Point out each Plasmodium parasite.
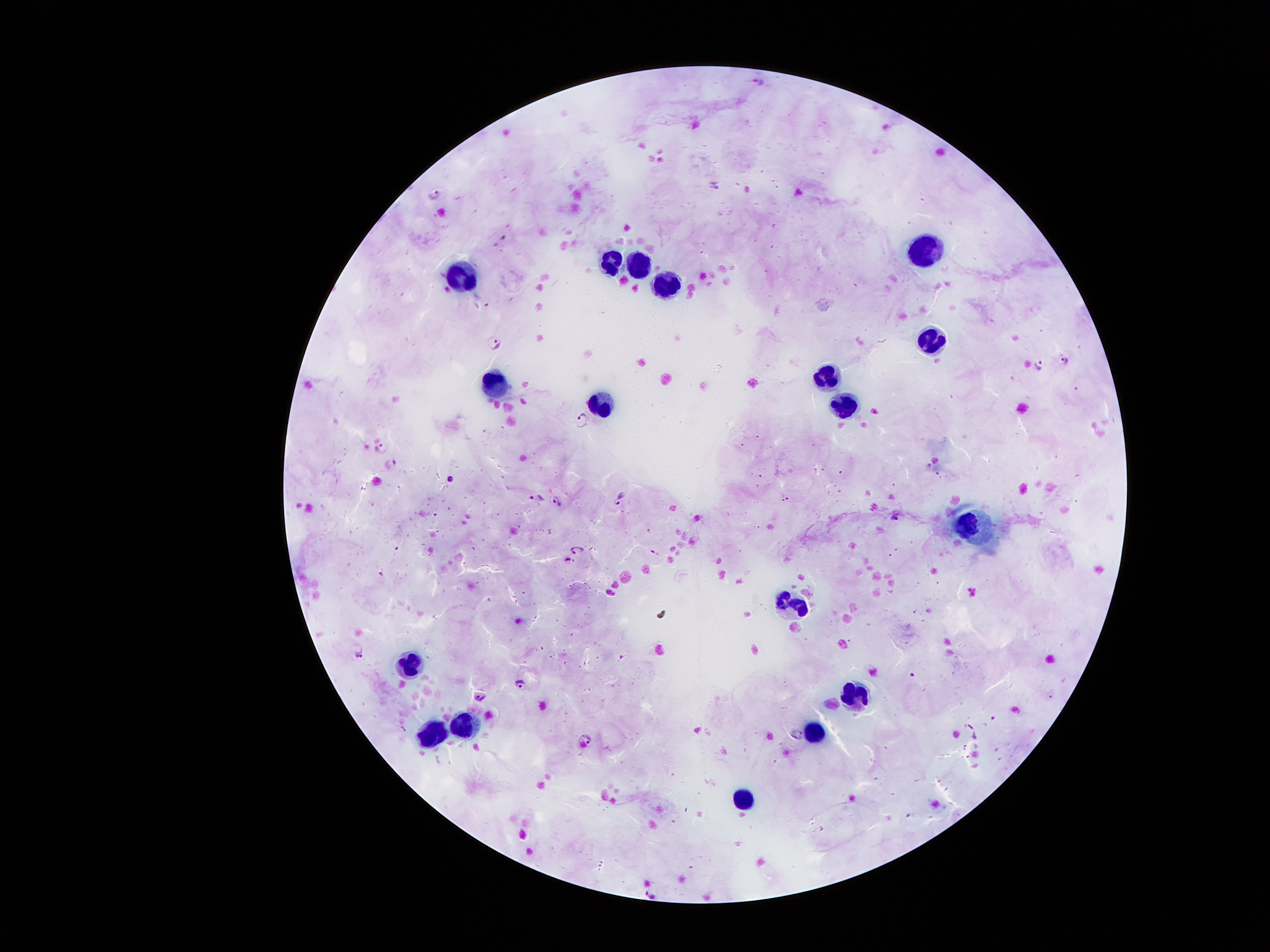

Approximate object centers, in pixels from the top-left corner.
Plasmodium parasites: (x=758, y=81), (x=713, y=183), (x=435, y=193), (x=495, y=341), (x=1064, y=360), (x=1039, y=364), (x=579, y=421), (x=384, y=450), (x=393, y=462), (x=536, y=497), (x=620, y=500), (x=558, y=503), (x=896, y=514), (x=577, y=550), (x=359, y=651), (x=519, y=683), (x=478, y=697), (x=585, y=741).

Summary:
  - Leukocyte locations: (x=931, y=250), (x=610, y=257), (x=640, y=263), (x=461, y=274), (x=670, y=283), (x=932, y=342), (x=831, y=372), (x=494, y=380), (x=601, y=400), (x=847, y=401), (x=967, y=520), (x=793, y=603), (x=407, y=665), (x=859, y=692), (x=461, y=718), (x=808, y=732), (x=433, y=735), (x=739, y=797)
  - Preparation: thick blood smear
  - Magnification: 100x
  - Capture: smartphone through the microscope eyepiece
  - Field of view: one from this slide
  - Stain: Giemsa
  - Patient malaria status: positive for Plasmodium falciparum
  - Image size: 1270×952 pixels